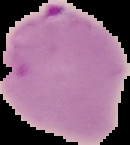 From a thin blood film. Result: malaria parasites detected. The area outside the segmented cell region is set to black. Image is 130×145 pixels.